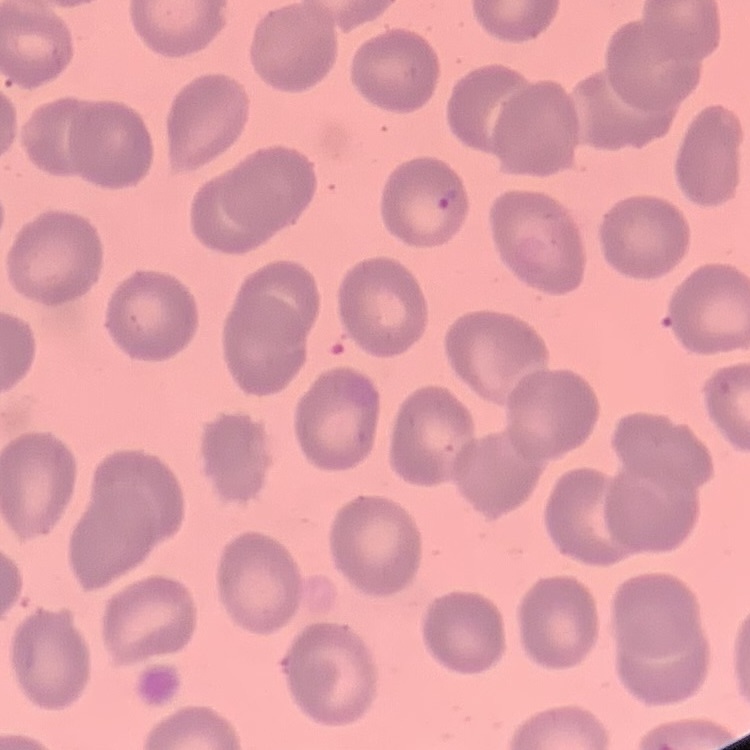

erythrocyte morphology = no rouleaux formation
preparation = thin blood smear
image type = square crop of a larger photomicrograph
stain = Field's or Giemsa